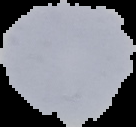

Summary:
  - Result: negative for malaria parasites
  - Image size: 136×127 pixels
  - Image type: segmented cell region with the area outside set to black
  - Preparation: thin blood smear